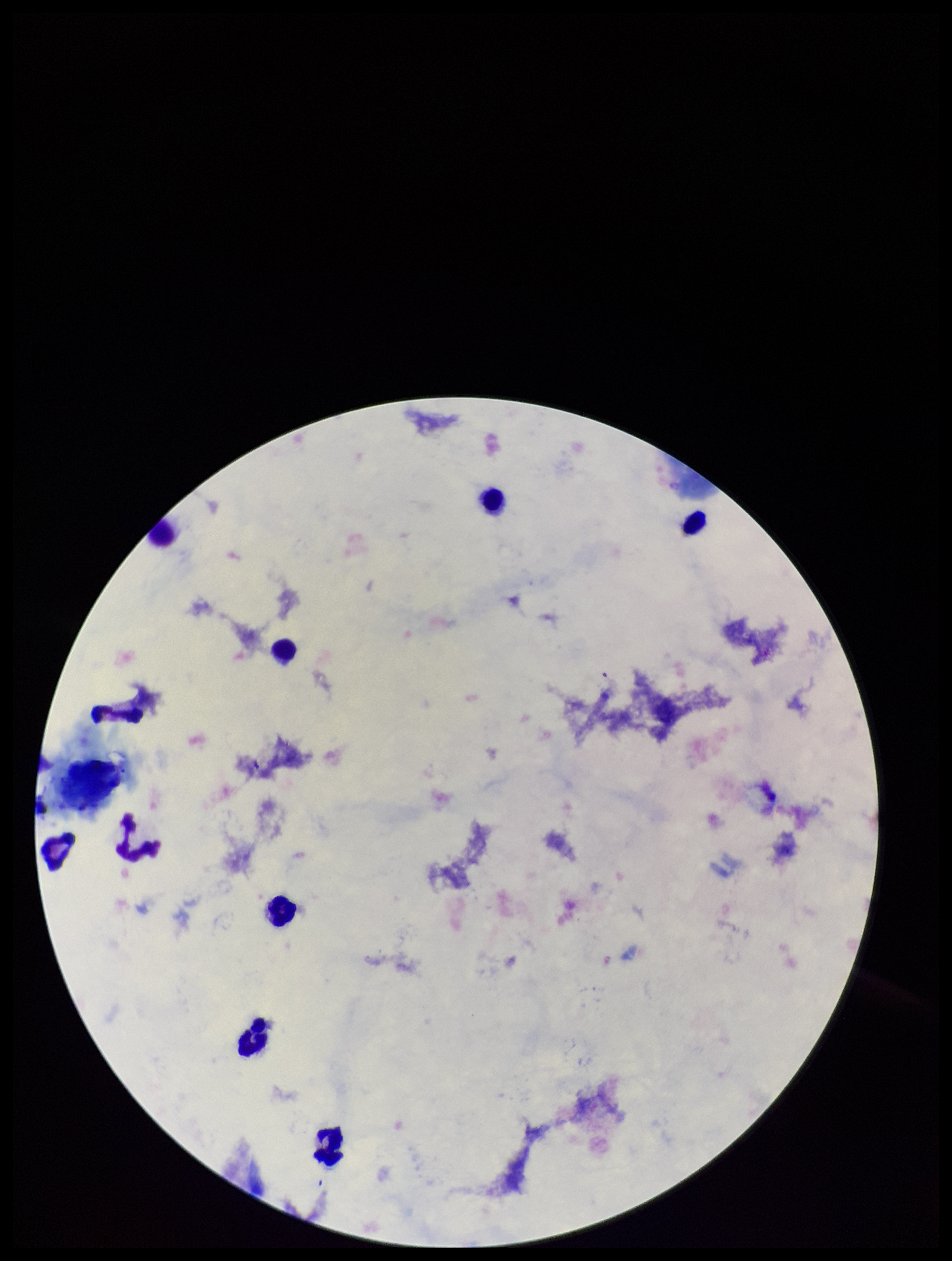

Parasite count: 0. Patient malaria status: negative. Smartphone photograph taken through the eyepiece of a microscope. Stained with Giemsa. Preparation: thick blood smear. Single field of view. Image is 952×1261 pixels. Leukocyte count: 8. Plasmodium parasites: none identified.